Locate every Plasmodium falciparum-infected red blood cell.
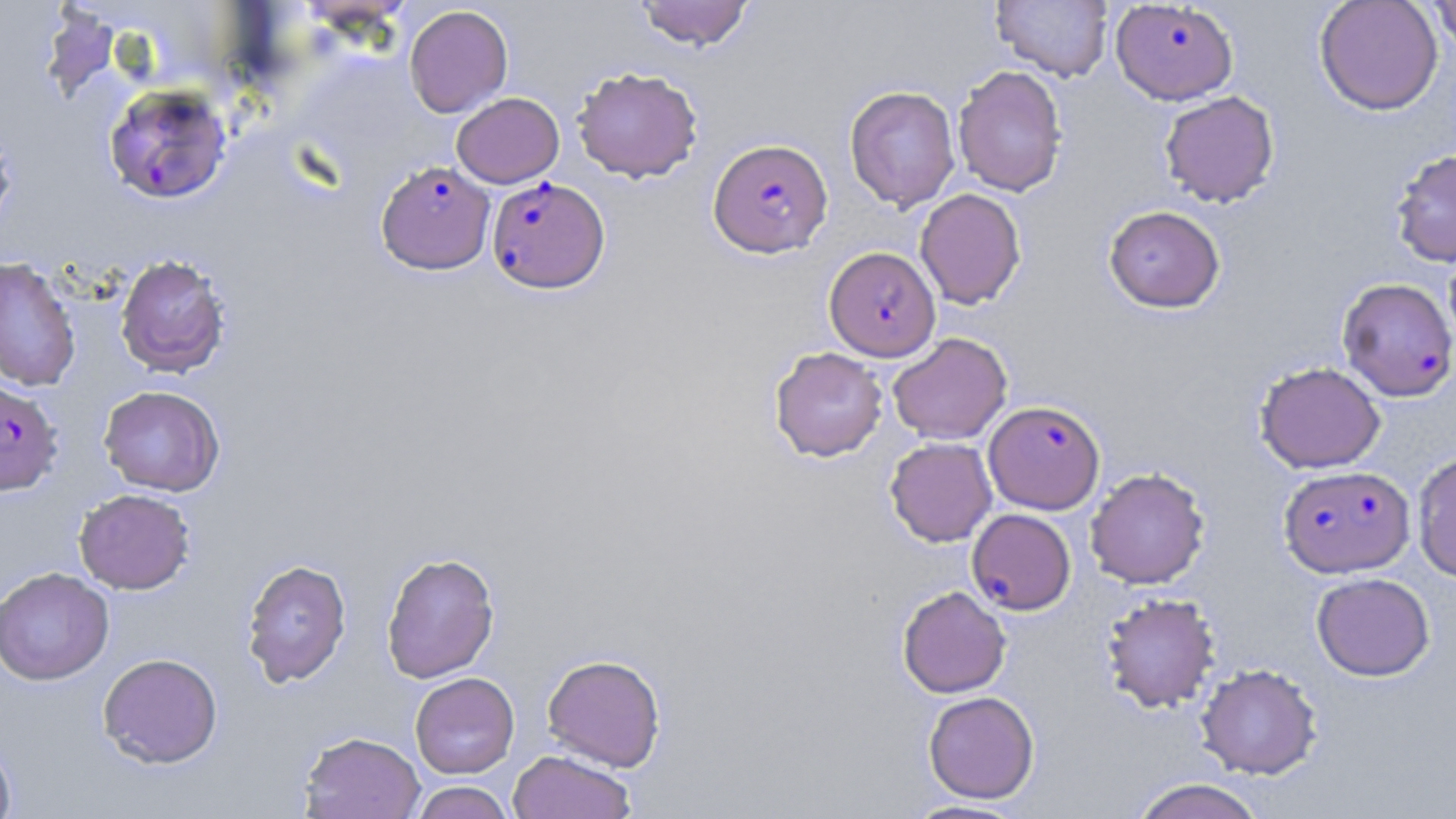
Approximate bounding boxes as (x1,y1)-(x2,y2) corner pairs in pixels.
Plasmodium falciparum-infected red blood cells: (1110,0)-(1238,105), (103,83)-(232,204), (708,137)-(833,257), (377,161)-(495,274), (487,177)-(610,294), (824,246)-(941,361), (1337,277)-(1456,402), (0,379)-(63,496), (983,400)-(1105,514), (1278,465)-(1414,577), (967,508)-(1076,615).

slide_level_diagnosis: Plasmodium falciparum
modality: light microscopy
image_size: 1456×819 pixels
stain: May-Grünwald-Giemsa
uninfected_red_blood_cell_locations: 'approximate bounding boxes as (x1,y1)-(x2,y2) corner pairs in pixels: (991,0)-(1114,82), (1314,0)-(1443,115), (1430,0)-(1456,54), (635,1)-(754,50), (40,5)-(121,103), (404,5)-(513,118), (953,65)-(1068,197), (572,66)-(703,183), (844,85)-(960,212), (1159,91)-(1280,208), (451,92)-(564,188), (0,122)-(16,238), (1389,148)-(1456,267), (915,188)-(1027,309), (1103,205)-(1225,313), (115,253)-(231,378), (0,257)-(81,392), (888,332)-(1012,445), (769,347)-(888,462), (1255,361)-(1386,473), (98,385)-(224,496), (884,437)-(997,547), (1411,450)-(1456,582), (1085,467)-(1210,589), (74,488)-(196,594), (381,552)-(500,683), (240,558)-(352,688), (0,566)-(115,685), (1311,572)-(1435,681), (897,585)-(1011,698), (1100,592)-(1221,714), (98,652)-(223,768), (542,653)-(666,772), (1195,662)-(1323,780), (410,672)-(519,778), (923,691)-(1039,804), (299,731)-(425,819), (0,737)-(17,819), (507,749)-(636,819), (1129,778)-(1268,819), (410,781)-(514,819), (905,799)-(1029,818)'
magnification: 1000x
preparation: thin blood film
field_of_view: one of a larger specimen